Name the parasite shown.
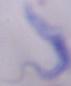
This is a trypanosome.

{
  "modality": "photomicrograph",
  "magnification": "1000x"
}